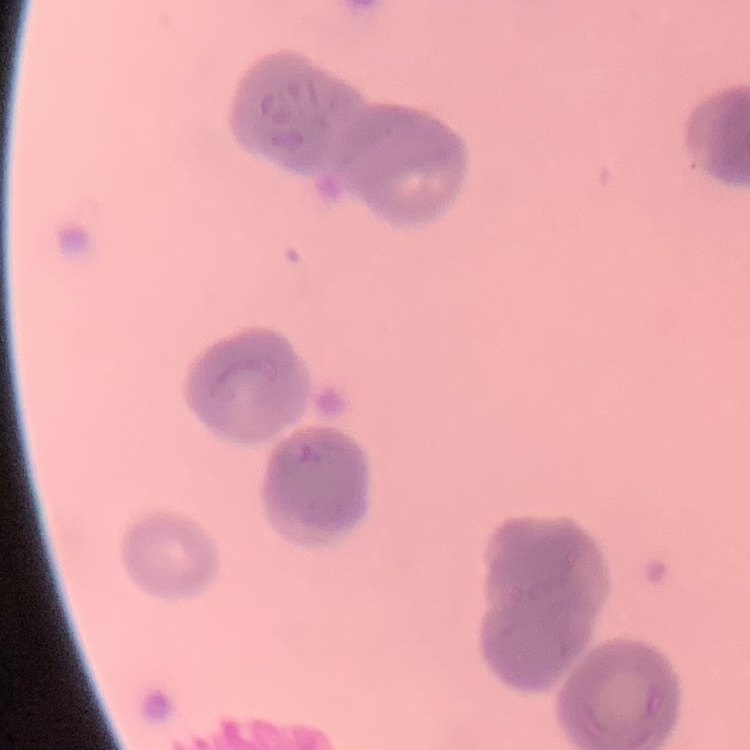
Summary:
  - Red blood cell morphology: rouleaux formation
  - Stain: Field's or Giemsa
  - Image type: square crop of a larger photomicrograph
  - Preparation: thin peripheral smear